Give the preparation type.
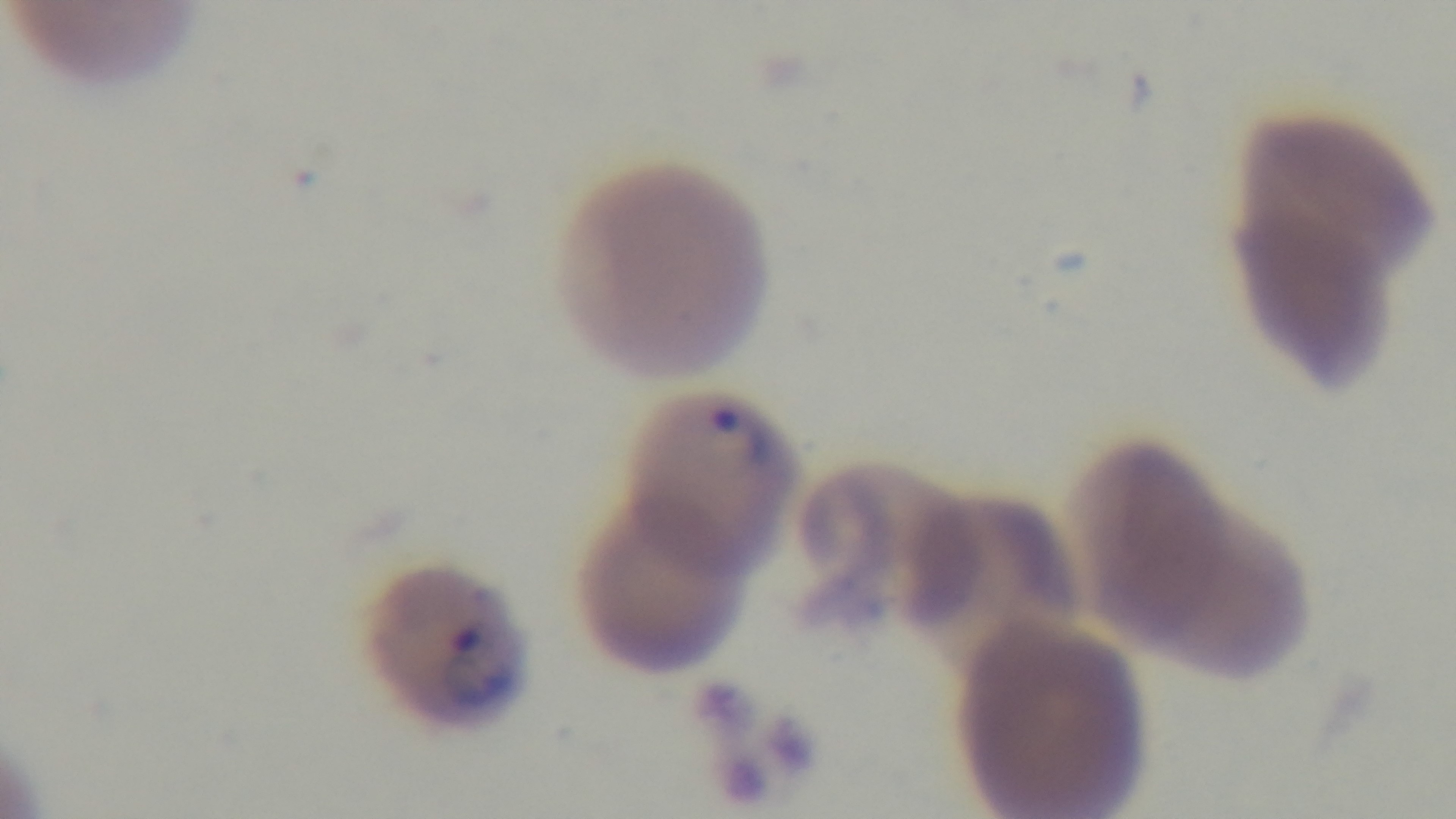

A thin smear.

Summary:
  - Malaria status: positive
  - Modality: light microscopy
  - Stain: Giemsa
  - Capture: mounted 4K digital camera
  - Objective: 100x oil immersion
  - Field of view: single